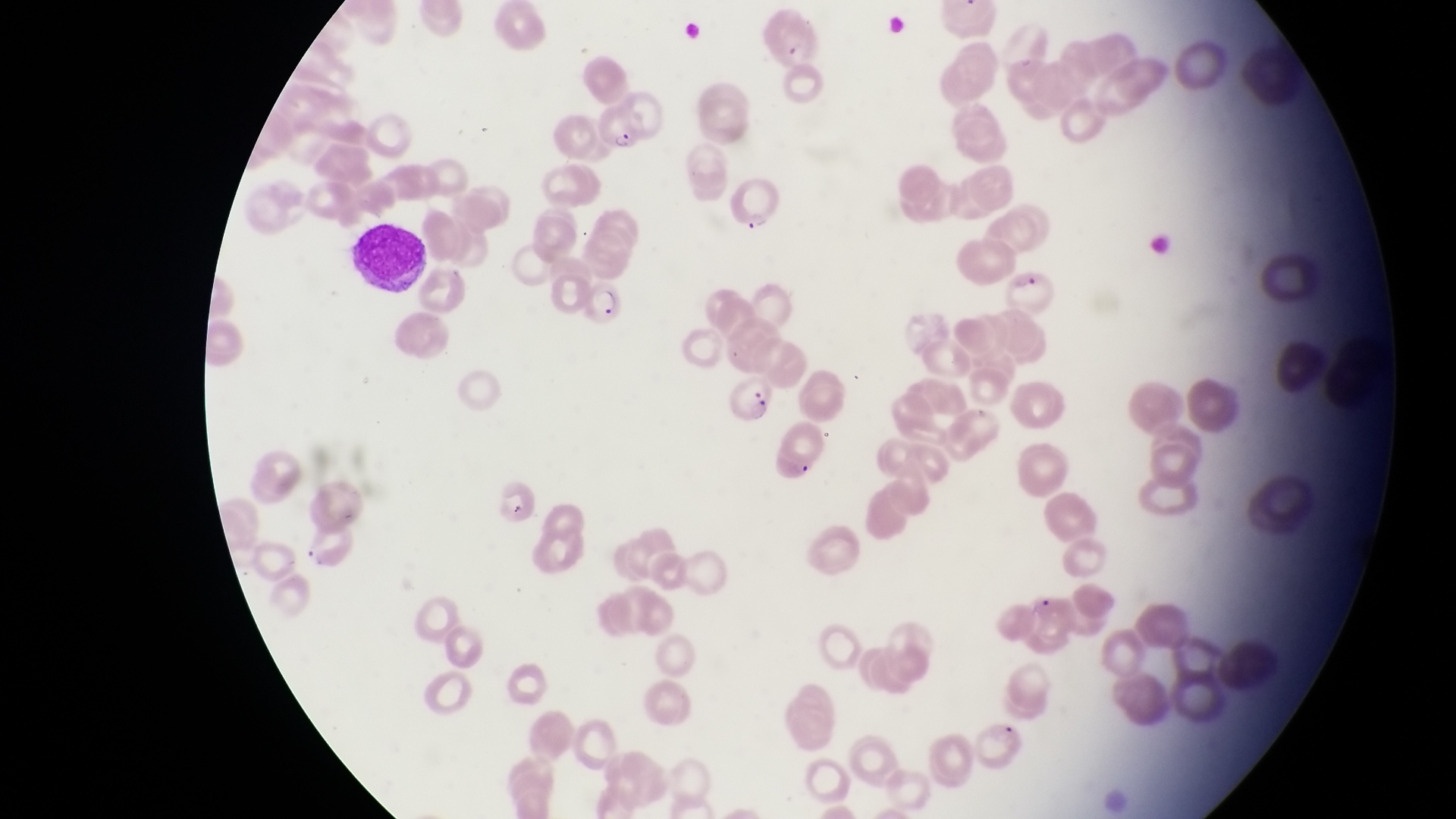

Approximate bounding boxes as left top right bottom in pixels.
Summary:
  - Leukocyte locations: 346 225 432 289
  - Parasitised red blood cell locations: 588 96 647 163; 723 171 781 231; 1003 268 1056 323; 578 278 624 321; 723 373 779 432
  - Field of view: single
  - Image size: 1456×819 pixels
  - Magnification: 1000x
  - Country: Uganda
  - Capture: smartphone photograph through the eyepiece of an Olympus CX-23 microscope
  - Preparation: thin blood smear